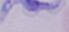
Summary:
  - Modality: photomicrograph
  - Magnification: 1000x
  - Identification: trypanosome